Classify this cell by malaria status.
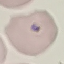

It is parasitized.

Giemsa-stained preparation. Acquired by smartphone through the microscope eyepiece. Automatically extracted cell patch, resized to 64 × 64 pixels. Thin blood smear.